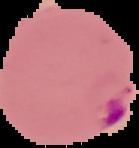
Summary:
  - Image size: 139×148 pixels
  - Result: malaria parasites detected
  - Preparation: thin blood smear
  - Image type: cell region segmented out of the field of view; surrounding area masked to black